Assess the morphology of the red blood cells.
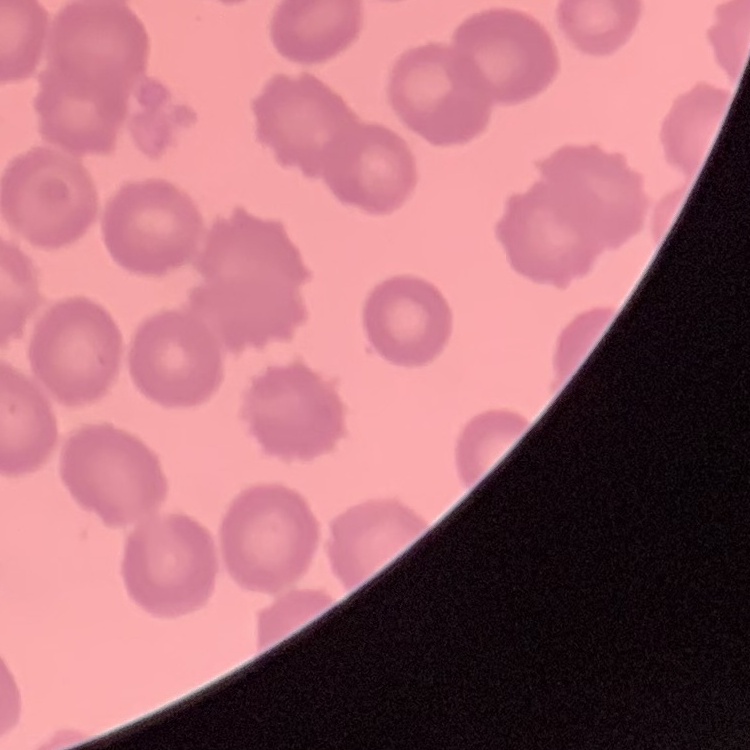

They show no rouleaux formation.

{
  "preparation": "thin blood smear",
  "image_type": "square crop of a larger photomicrograph",
  "stain": "Field's or Giemsa"
}